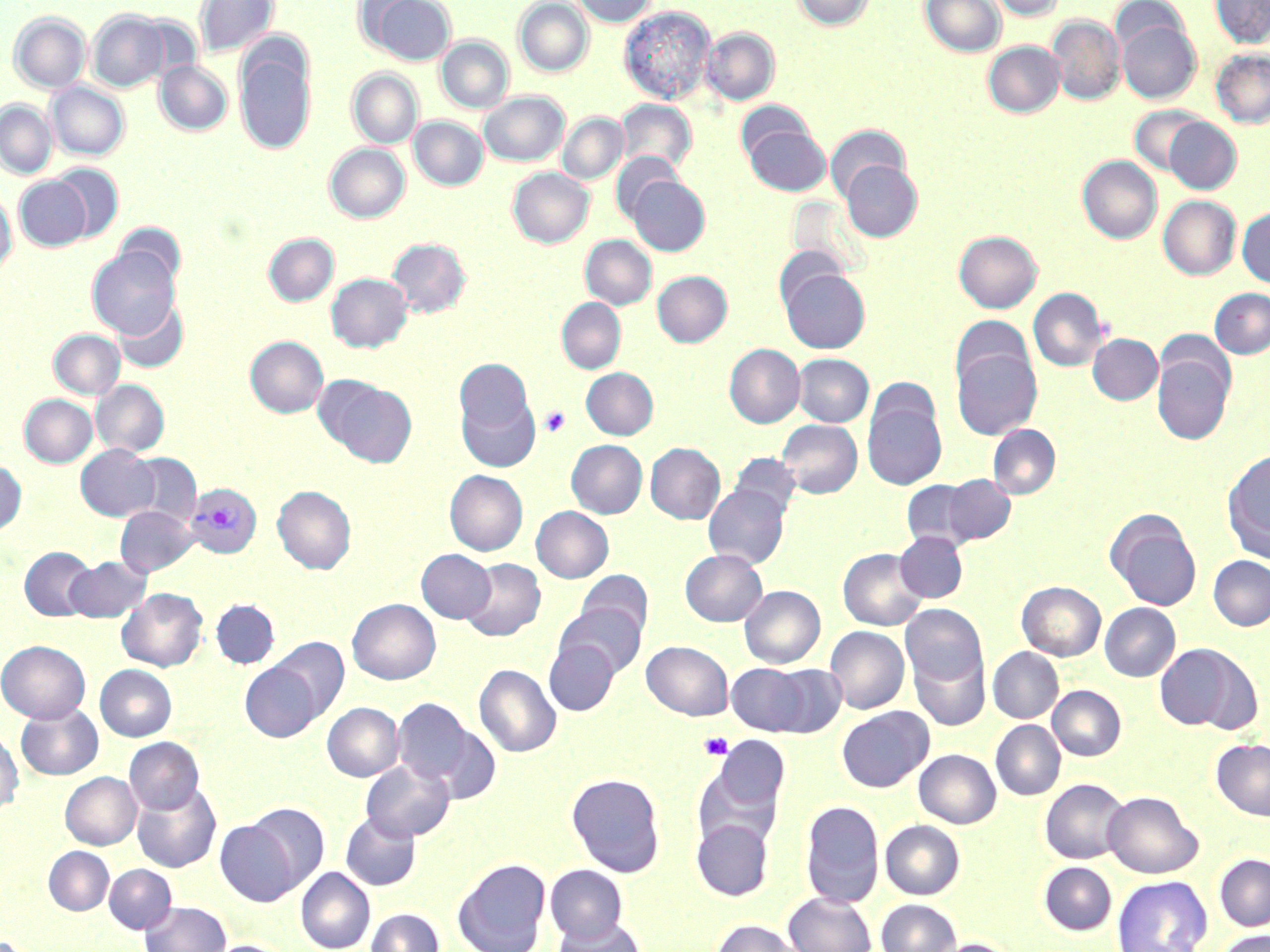
slide-level diagnosis = Plasmodium vivax
magnification = 1000x
Plasmodium vivax-infected red blood cell locations = approximate bounding boxes as [x1, y1, x2, y2] in pixels: [185, 484, 262, 558]
stain = May-Grünwald-Giemsa
uninfected red blood cell locations = approximate bounding boxes as [x1, y1, x2, y2] in pixels: [195, 0, 278, 58], [367, 0, 457, 65], [514, 0, 593, 77], [570, 0, 657, 27], [792, 0, 874, 30], [920, 0, 1006, 57], [987, 0, 1065, 20], [1211, 0, 1270, 49], [619, 6, 716, 104], [87, 10, 169, 92], [10, 12, 91, 93], [1047, 15, 1125, 105], [1116, 18, 1201, 103], [702, 28, 779, 105], [234, 36, 316, 156], [437, 36, 513, 113], [983, 41, 1064, 118], [1211, 49, 1270, 129], [155, 61, 232, 135], [347, 69, 422, 149], [47, 82, 128, 160], [479, 91, 569, 166], [616, 99, 697, 174], [0, 100, 57, 178], [1128, 106, 1207, 176], [558, 113, 627, 184], [410, 116, 488, 190], [1163, 118, 1241, 194], [743, 123, 830, 196], [825, 125, 909, 203], [325, 143, 409, 222], [611, 152, 682, 224], [1077, 155, 1162, 245], [840, 159, 922, 241], [49, 162, 125, 241], [508, 167, 593, 248], [14, 176, 91, 252], [627, 176, 710, 256], [0, 187, 16, 275], [1158, 195, 1241, 279], [1237, 207, 1270, 289], [114, 223, 186, 289], [954, 231, 1042, 313], [264, 233, 338, 306], [581, 235, 656, 310], [387, 238, 471, 317], [87, 246, 180, 338], [781, 268, 870, 353], [653, 271, 732, 346], [327, 273, 412, 352], [1028, 288, 1107, 372], [1210, 288, 1270, 358], [113, 298, 188, 373], [557, 298, 625, 373], [49, 329, 124, 399], [1088, 334, 1162, 404], [245, 336, 328, 418], [724, 343, 805, 428], [1152, 343, 1236, 446], [951, 344, 1042, 440], [793, 354, 873, 427], [454, 358, 534, 440], [581, 367, 658, 439], [316, 376, 417, 467], [92, 380, 169, 456], [457, 384, 539, 473], [19, 395, 97, 467], [862, 397, 946, 490], [776, 419, 862, 498], [988, 425, 1060, 499], [566, 440, 647, 518], [646, 443, 725, 524], [76, 445, 160, 520], [1221, 449, 1270, 563], [124, 453, 203, 528], [729, 453, 801, 521], [0, 460, 26, 536], [445, 470, 527, 556], [943, 475, 1015, 545], [901, 480, 977, 549], [703, 483, 790, 570], [273, 485, 356, 574], [116, 506, 198, 577], [532, 506, 613, 582], [1105, 509, 1202, 611], [895, 531, 967, 602], [19, 547, 97, 621], [838, 548, 927, 630], [416, 549, 495, 623], [680, 549, 767, 626], [1208, 555, 1270, 630], [65, 556, 150, 623], [461, 558, 545, 640], [576, 570, 652, 641], [1017, 581, 1105, 660], [740, 585, 825, 668], [117, 588, 207, 671], [212, 599, 279, 668], [347, 599, 440, 684], [1100, 603, 1180, 681], [556, 604, 646, 679], [901, 604, 987, 687], [825, 626, 909, 714], [269, 637, 349, 723], [0, 640, 89, 723], [544, 640, 619, 715], [642, 641, 733, 720], [1154, 642, 1257, 733], [988, 647, 1063, 723], [909, 648, 990, 731], [240, 662, 323, 742], [726, 663, 814, 736], [765, 663, 847, 737], [474, 664, 561, 757], [95, 665, 176, 740], [1048, 686, 1125, 761], [393, 698, 477, 787], [16, 701, 103, 781], [322, 702, 403, 781], [836, 706, 934, 792], [991, 720, 1065, 800], [425, 722, 502, 804], [0, 729, 23, 816], [709, 736, 790, 820], [124, 737, 204, 815], [1211, 739, 1270, 821], [914, 749, 1001, 828], [694, 759, 783, 848], [361, 760, 455, 841], [60, 772, 141, 849], [566, 772, 666, 877], [1040, 779, 1129, 864], [132, 782, 221, 873], [1103, 791, 1203, 878], [800, 800, 884, 908], [244, 802, 329, 889], [341, 812, 421, 890], [692, 818, 773, 901], [216, 819, 301, 906], [881, 820, 965, 899], [44, 846, 114, 915], [1214, 853, 1270, 931], [452, 857, 550, 952], [1039, 862, 1117, 935], [104, 864, 177, 933], [544, 864, 628, 945], [296, 868, 375, 952], [1112, 876, 1212, 952], [783, 892, 876, 952], [877, 899, 960, 952], [140, 901, 231, 952], [367, 908, 444, 952], [553, 917, 645, 952], [710, 919, 804, 952], [1215, 930, 1270, 952], [932, 938, 1019, 952], [203, 940, 293, 952]
modality = optical microscopy
image size = 1270×952 pixels
field of view = single
platelet locations = approximate bounding boxes as [x1, y1, x2, y2] in pixels: [540, 407, 571, 436], [699, 732, 733, 760]
preparation = thin blood smear